Describe the morphology of the red blood cells.
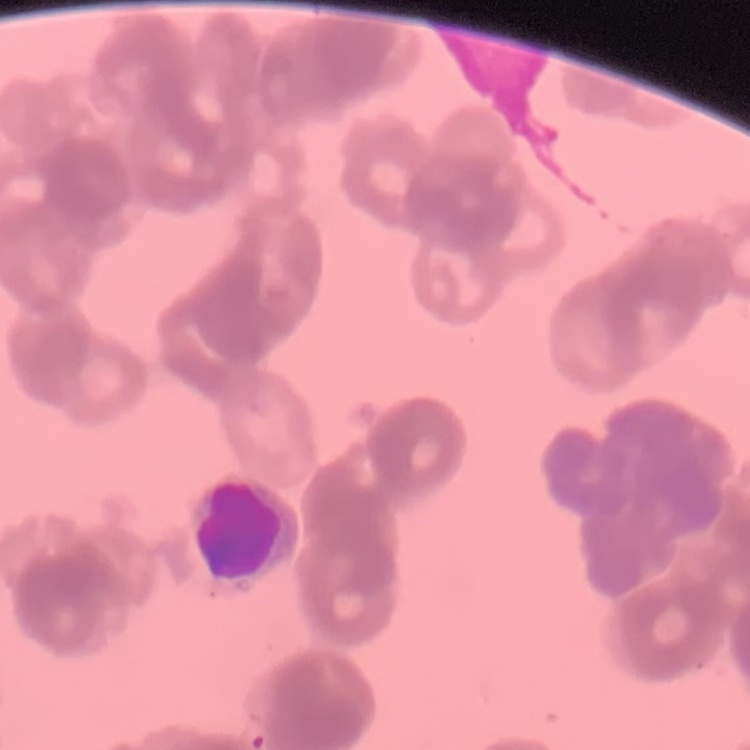
They show rouleaux formation.

Stained with either Field's or Giemsa. Thin peripheral smear. Square crop of a larger photomicrograph.